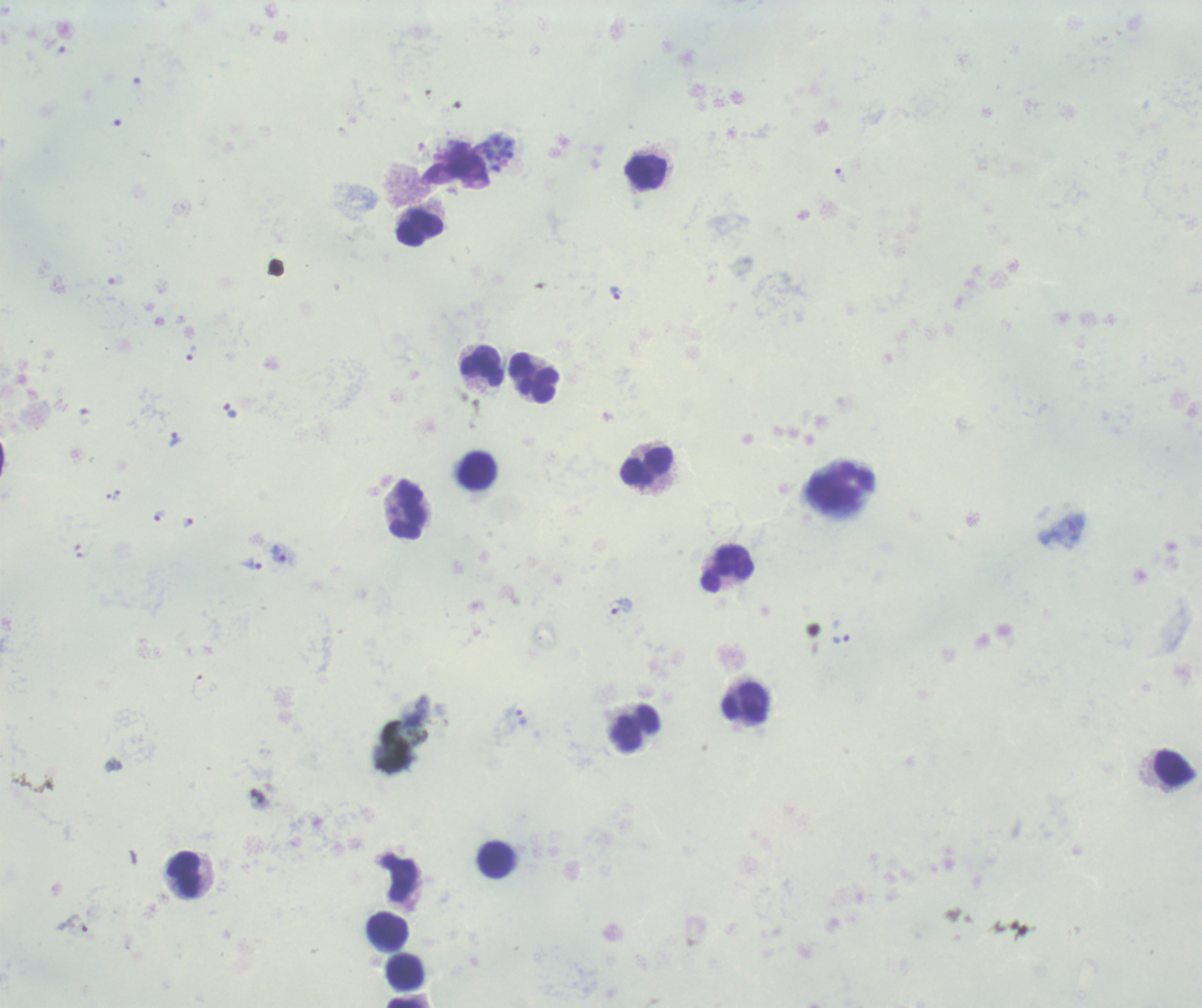

Approximate centers as (x, y) in pixels. Leukocyte locations: (646, 172), (420, 229), (482, 366), (533, 377), (645, 466), (477, 470), (408, 508), (727, 569), (746, 703), (636, 728), (1175, 768), (496, 859), (183, 874), (388, 931), (405, 971), (404, 1003). Trophozoite locations: (840, 176), (615, 294), (191, 352), (174, 439), (116, 495), (158, 516), (187, 522), (279, 553), (251, 564), (621, 606), (841, 638), (521, 717). Schizont locations: (497, 153). Life-cycle stages observed: trophozoite, schizont. Single field of view. Previously used in a real diagnosis. Image is 1202×1008 pixels. Result: positive for malaria parasites. 100x magnification. Romanowsky stain. Background quality: unsatisfactory. Thick blood smear.